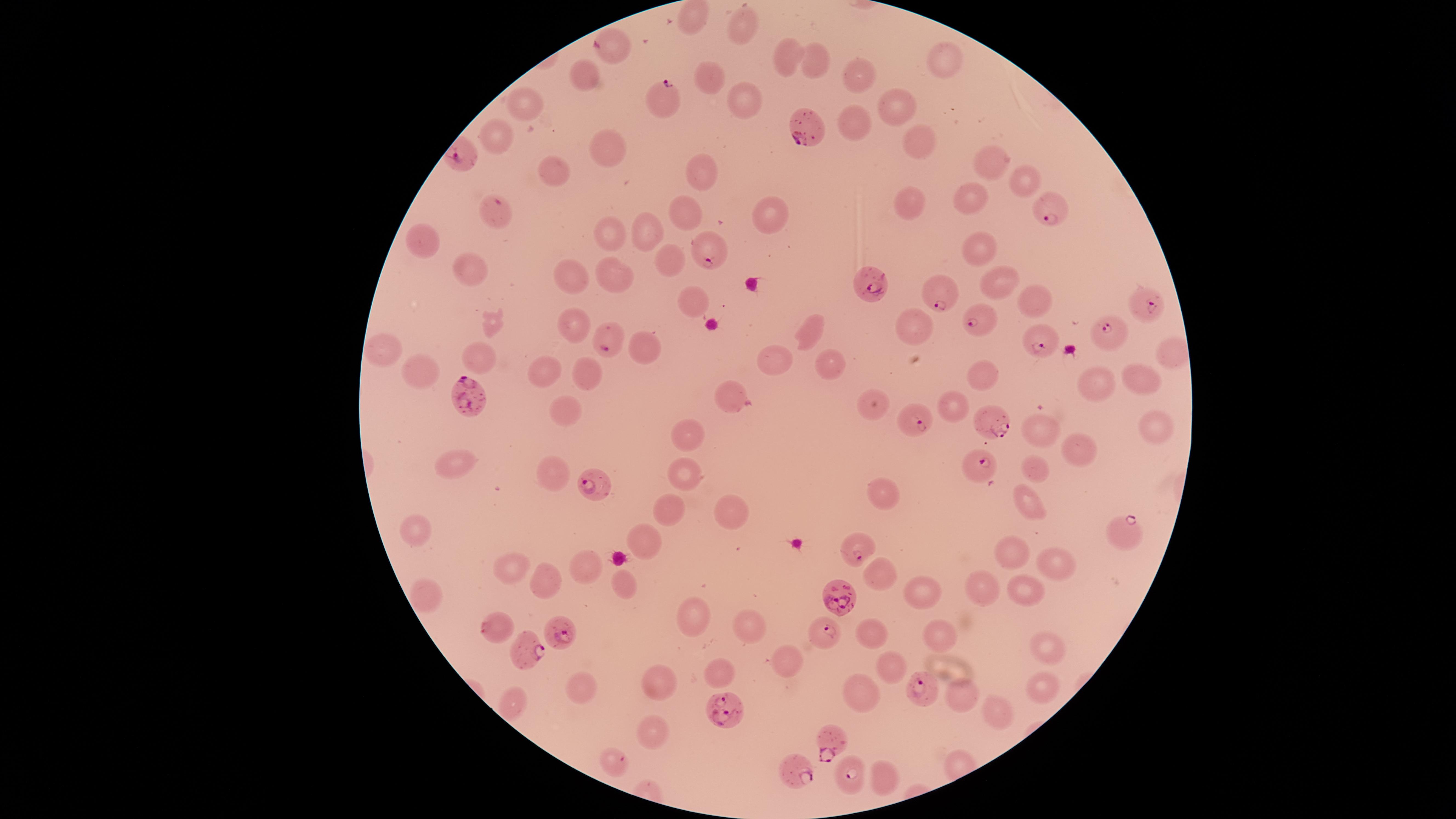 Approximate marker points, in pixels from the top-left corner. Parasitized red blood cells: (x=614, y=44), (x=659, y=100), (x=810, y=127), (x=496, y=211), (x=1053, y=211), (x=709, y=259), (x=877, y=284), (x=939, y=294), (x=1145, y=306), (x=982, y=318), (x=1108, y=329), (x=606, y=337), (x=1039, y=341), (x=473, y=398), (x=922, y=421), (x=994, y=421), (x=980, y=468), (x=597, y=486), (x=1120, y=528), (x=856, y=548), (x=837, y=596), (x=494, y=627), (x=564, y=629), (x=821, y=631), (x=525, y=650), (x=919, y=689), (x=724, y=714), (x=832, y=740), (x=615, y=764), (x=795, y=771), (x=851, y=782). Uninfected red blood cells: (x=742, y=25), (x=786, y=51), (x=947, y=59), (x=813, y=66), (x=859, y=73), (x=706, y=76), (x=585, y=78), (x=741, y=99), (x=896, y=109), (x=524, y=110), (x=854, y=120), (x=500, y=135), (x=915, y=144), (x=605, y=152), (x=989, y=164), (x=704, y=174), (x=553, y=175), (x=1023, y=179), (x=973, y=203), (x=910, y=207), (x=691, y=211), (x=771, y=216), (x=640, y=229), (x=605, y=236), (x=421, y=241), (x=983, y=251), (x=673, y=266), (x=471, y=268), (x=574, y=275), (x=613, y=276), (x=994, y=281), (x=690, y=301), (x=1031, y=302), (x=579, y=324), (x=919, y=328), (x=809, y=329), (x=633, y=346), (x=1171, y=347), (x=384, y=350), (x=479, y=357), (x=776, y=366), (x=548, y=370), (x=828, y=370), (x=590, y=373), (x=420, y=376), (x=981, y=380), (x=1142, y=380), (x=1094, y=386), (x=730, y=390), (x=872, y=403), (x=569, y=409), (x=952, y=409), (x=1155, y=426), (x=1037, y=430), (x=687, y=438), (x=1080, y=447), (x=1036, y=467), (x=455, y=470), (x=552, y=477), (x=682, y=477), (x=884, y=486), (x=1023, y=502), (x=733, y=505), (x=669, y=510), (x=414, y=535), (x=646, y=540), (x=1013, y=550), (x=1056, y=562), (x=581, y=564), (x=516, y=568), (x=879, y=579), (x=551, y=584), (x=621, y=586), (x=1022, y=587), (x=921, y=588), (x=984, y=589), (x=423, y=592), (x=695, y=618), (x=751, y=629), (x=870, y=637), (x=941, y=639), (x=1043, y=645), (x=718, y=665), (x=789, y=668), (x=889, y=668), (x=662, y=684), (x=1034, y=687), (x=581, y=688), (x=863, y=694), (x=961, y=697), (x=994, y=709), (x=650, y=734), (x=884, y=777). Species: Plasmodium falciparum. Giemsa-stained preparation. Smartphone photograph through the microscope eyepiece. Presence: malaria parasites identified. Thin blood smear. Single field of view. Circular visible region. Image is 1456×819 pixels.